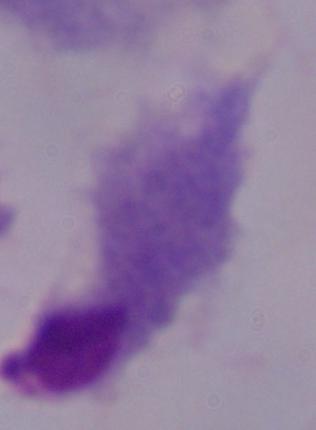
Summary:
  - Modality: micrograph
  - Identification: trichomonad
  - Magnification: 1000x